Classify this cell by malaria status.
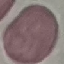
It is uninfected.

Summary:
  - Stain: Giemsa
  - Preparation: thin smear
  - Capture: smartphone through the microscope eyepiece
  - Image type: automatically extracted cell patch, resized to 64 × 64 pixels